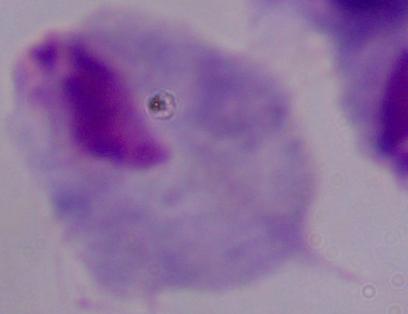
identification = trichomonad
magnification = 1000x
modality = photomicrograph